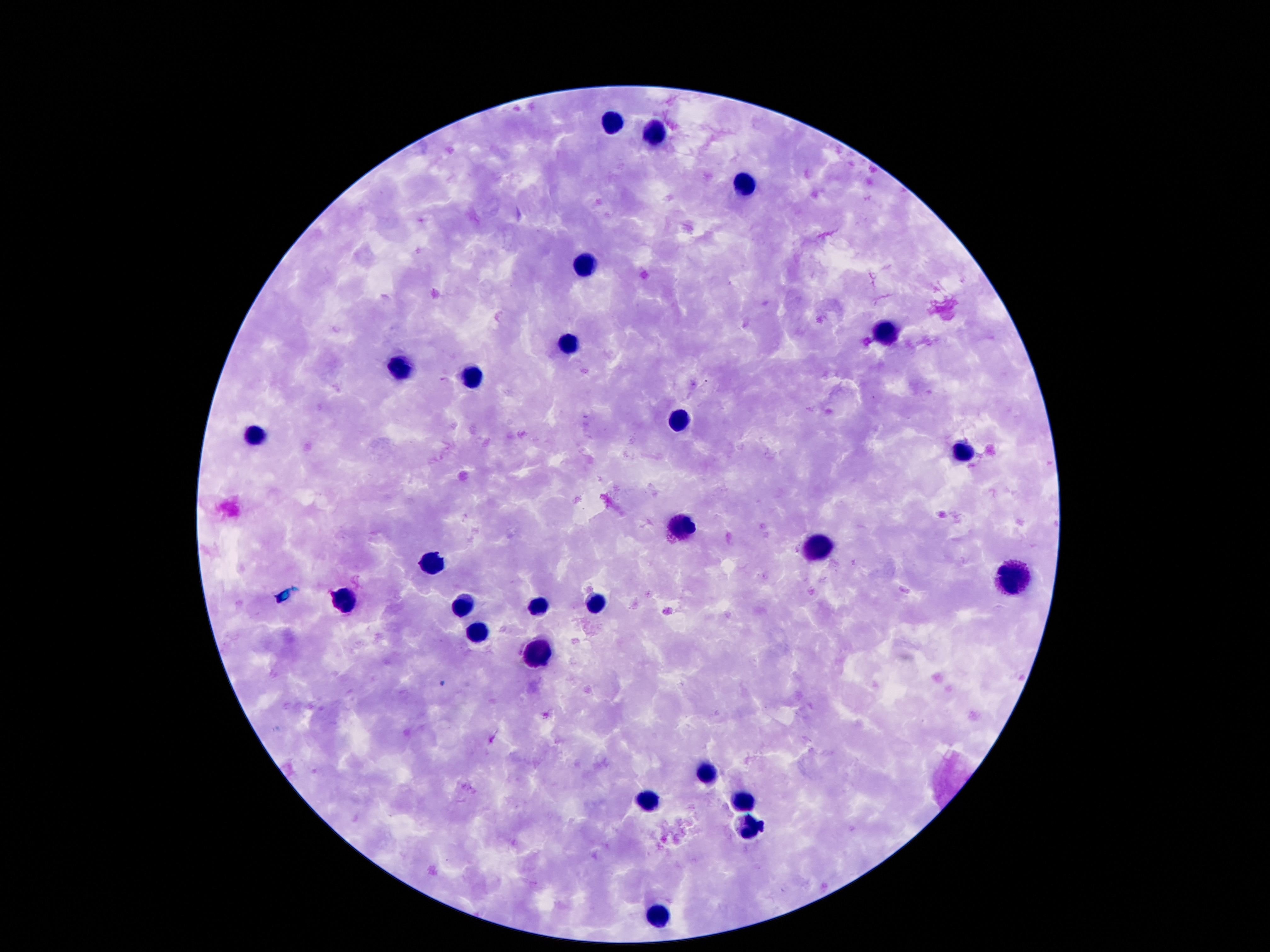
magnification = 100x
stain = Giemsa
capture = smartphone camera through the microscope eyepiece
field of view = single
preparation = thick peripheral-blood smear
image size = 1270×952 pixels
leukocyte locations = approximate object centers, in pixels from the top-left corner: (x=610, y=124), (x=656, y=133), (x=741, y=185), (x=586, y=265), (x=883, y=333), (x=568, y=340), (x=400, y=368), (x=474, y=375), (x=678, y=422), (x=257, y=434), (x=964, y=455), (x=682, y=524), (x=820, y=549), (x=433, y=565), (x=1014, y=577), (x=594, y=601), (x=349, y=602), (x=535, y=603), (x=461, y=606), (x=475, y=638), (x=537, y=652), (x=706, y=771), (x=649, y=801), (x=741, y=805), (x=748, y=826), (x=657, y=910)
patient malaria status = negative